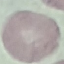
Malaria status: uninfected. Automatically extracted cell patch, resized to 64 × 64 pixels. Photographed with a smartphone camera at the microscope eyepiece. Giemsa-stained preparation. Thin blood smear.